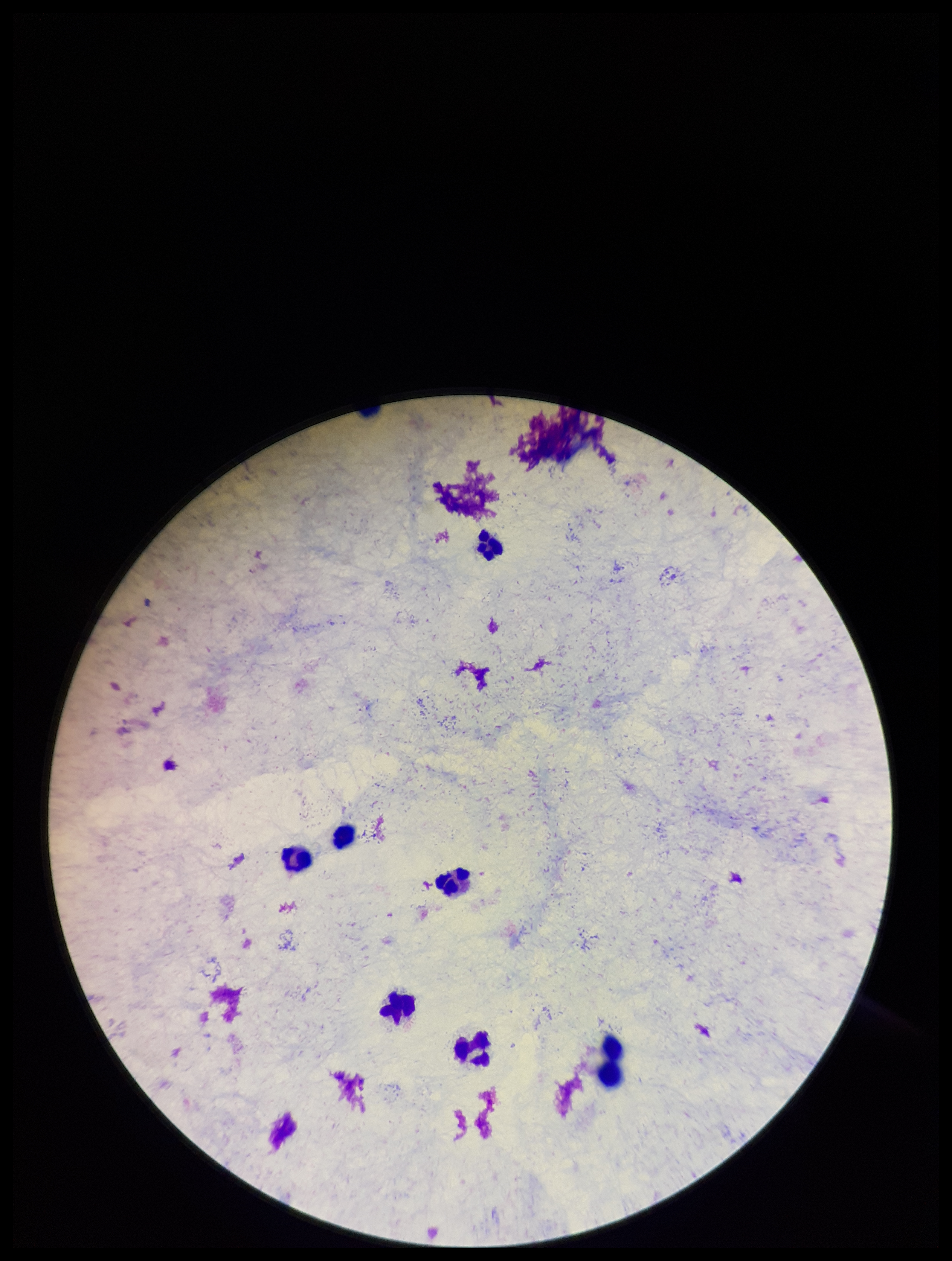 Parasite count: 0. Image is 952×1261 pixels. Plasmodium parasites: none identified. Leukocyte count: 7. Patient malaria status: negative. Photographed through the microscope eyepiece with a smartphone camera. Single field of view. Preparation: thick blood smear. Giemsa stain.